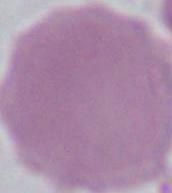

identification: erythrocyte
magnification: 1000x
modality: micrograph